Name the parasite shown.
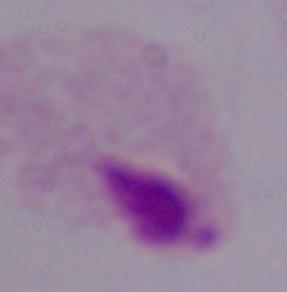
This is a trichomonad.

magnification = 1000x
modality = micrograph